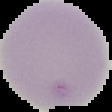
preparation = thin blood film
image type = segmented cell region with the area outside set to black
malaria status = uninfected
image size = 112×112 pixels